Assess the morphology of the erythrocytes.
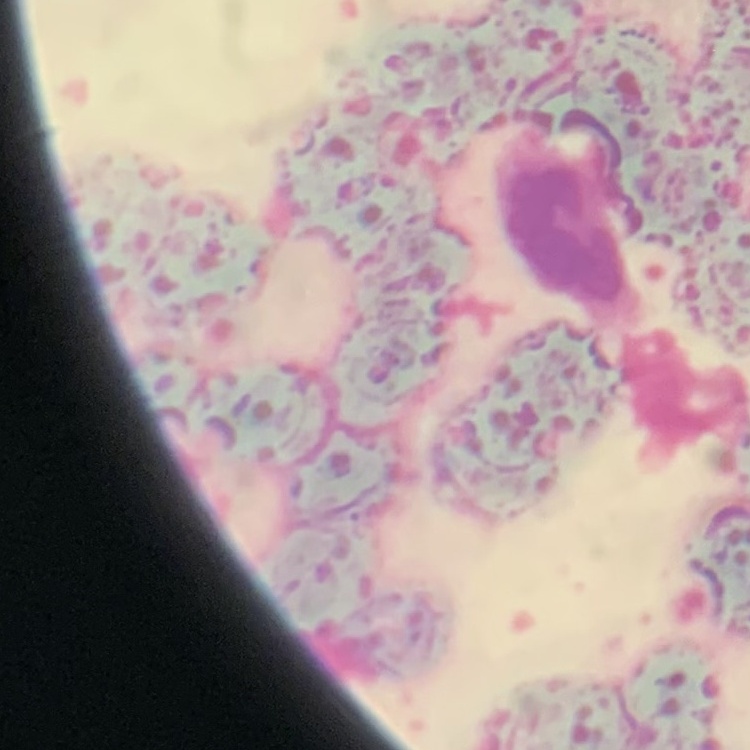

They show rouleaux formation.

Stained with either Field's or Giemsa. One tile cut from a larger photomicrograph. Thin peripheral smear.